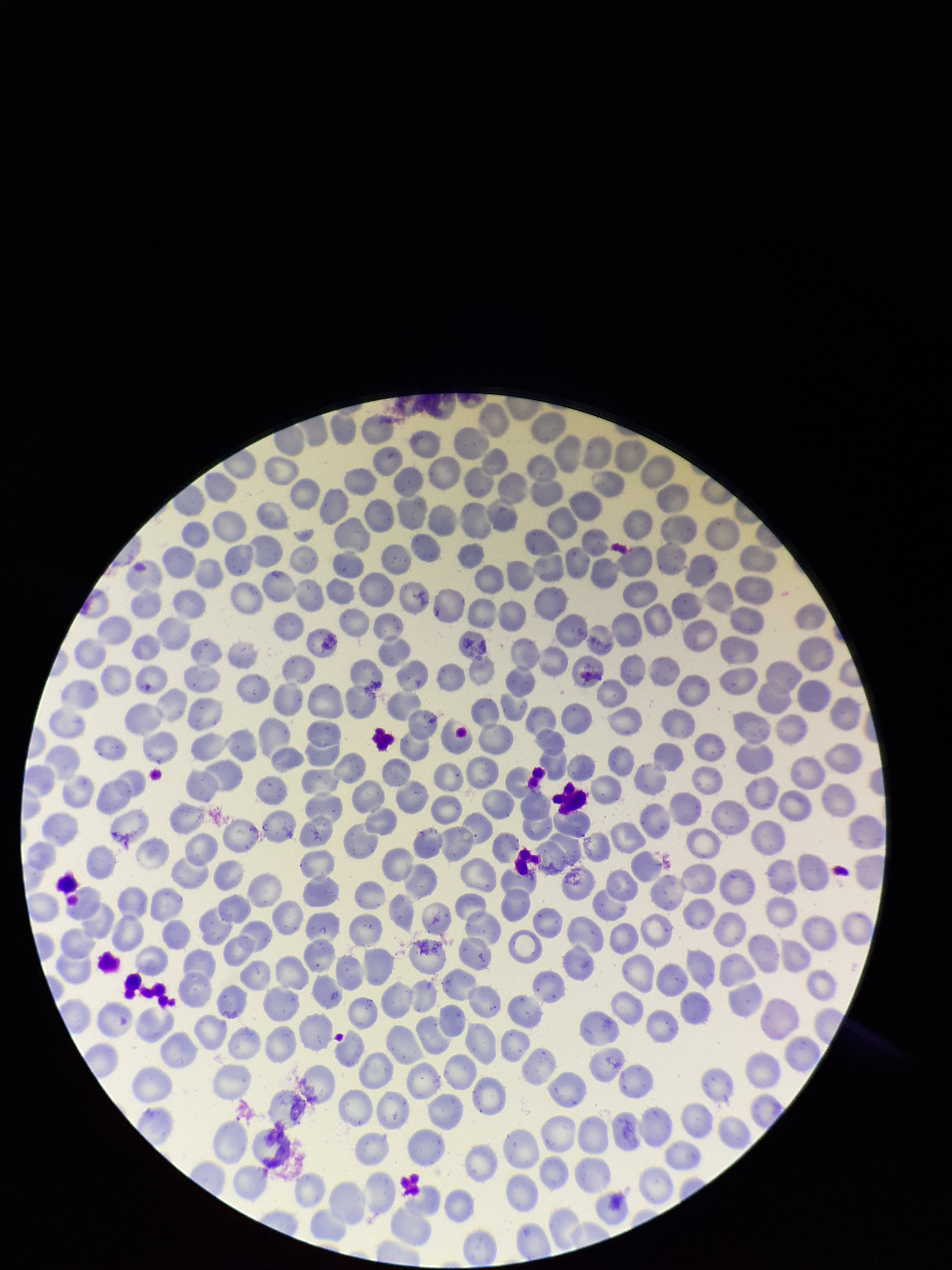 Preparation: thin. Image is 952×1270 pixels. Patient malaria status: negative. Parasitized red blood cells: none identified. Red blood cell count: 237. One field from this slide. Parasitized red blood cell count: 0. Photographed through the microscope eyepiece with a smartphone camera. Stained with Giemsa.